Identify the parasite.
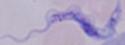

This is a trypanosome.

Summary:
  - Modality: micrograph
  - Magnification: 1000x